State which cell type is depicted.
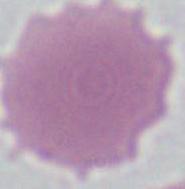

An erythrocyte.

{
  "magnification": "1000x",
  "modality": "photomicrograph"
}